Locate and identify every blood parasite.
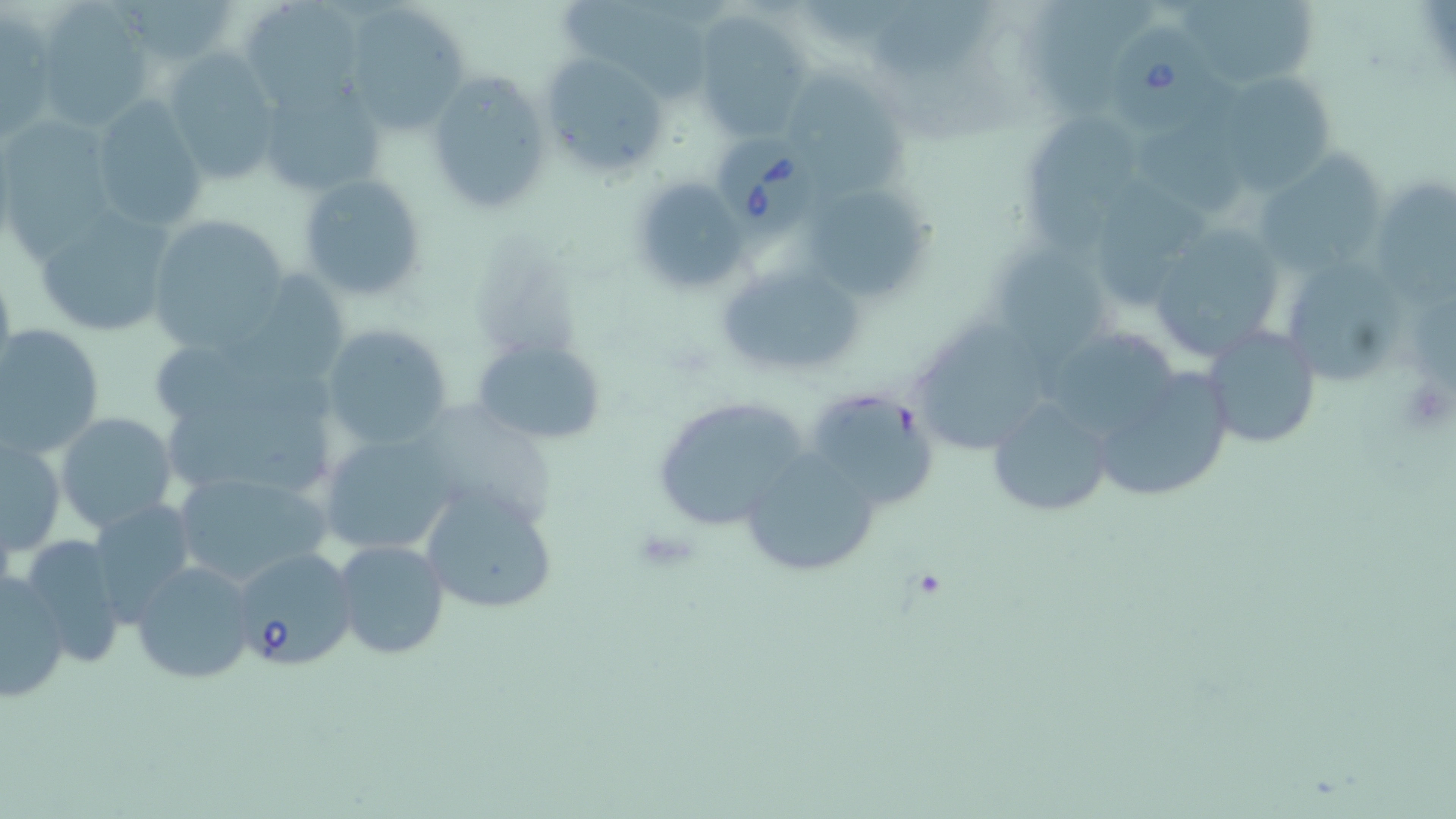
Approximate bounding boxes as (x1,y1)-(x2,y2) corner pairs in pixels.
Babesia divergens-infected red blood cells: (1107,18)-(1218,139), (719,132)-(819,233), (228,545)-(358,672).
No Plasmodium falciparum, Plasmodium ovale, Plasmodium malariae, Plasmodium vivax, or Trypanosoma brucei observed.

Uninfected red blood cell locations: (236,0)-(368,111), (565,0)-(714,107), (1040,0)-(1155,110), (1179,0)-(1317,91), (34,4)-(155,128), (341,4)-(473,133), (2,13)-(53,139), (694,13)-(814,142), (164,51)-(283,185), (540,53)-(670,179), (425,69)-(553,217), (1213,70)-(1336,193), (788,74)-(910,198), (255,75)-(383,199), (88,97)-(211,232), (1027,116)-(1146,250), (2,120)-(116,254), (1138,126)-(1251,222), (1252,146)-(1385,283), (297,174)-(431,303), (627,176)-(747,294), (1380,176)-(1456,308), (800,180)-(931,304), (1103,181)-(1201,308), (28,205)-(178,339), (146,214)-(291,350), (1142,222)-(1293,360), (989,249)-(1118,364), (1289,255)-(1401,389), (715,261)-(863,379), (224,275)-(347,390), (916,313)-(1056,456), (0,323)-(106,459), (321,323)-(454,453), (1200,324)-(1322,450), (1038,337)-(1182,440), (471,338)-(607,443), (153,339)-(338,443), (1085,365)-(1235,505), (803,390)-(937,510), (651,395)-(813,529), (985,395)-(1113,519), (56,411)-(177,532), (167,413)-(341,500), (316,430)-(459,558), (2,436)-(67,556), (739,451)-(885,576), (171,466)-(333,589), (419,485)-(558,616), (87,498)-(199,622), (15,531)-(131,668), (333,539)-(450,660), (131,560)-(256,684), (0,572)-(71,702). Slide-level diagnosis: Babesia divergens. Captured at 1000x magnification. May-Grünwald-Giemsa stain. Image is 1456×819 pixels. Optical microscopy. Thin blood smear. One field of a larger specimen.